Assess this cell for malaria.
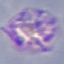
Parasitized.

image type = cell patch, automatically extracted from a larger field of view and resized to 64 × 64 pixels
preparation = thin blood smear
stain = Giemsa
capture = smartphone camera at the microscope eyepiece